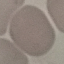
Summary:
  - Malaria status: uninfected
  - Preparation: thin blood smear
  - Capture: smartphone through the microscope eyepiece
  - Image type: cell patch, automatically extracted from a larger field of view and resized to 64 × 64 pixels
  - Stain: Giemsa